Identify the preparation type.
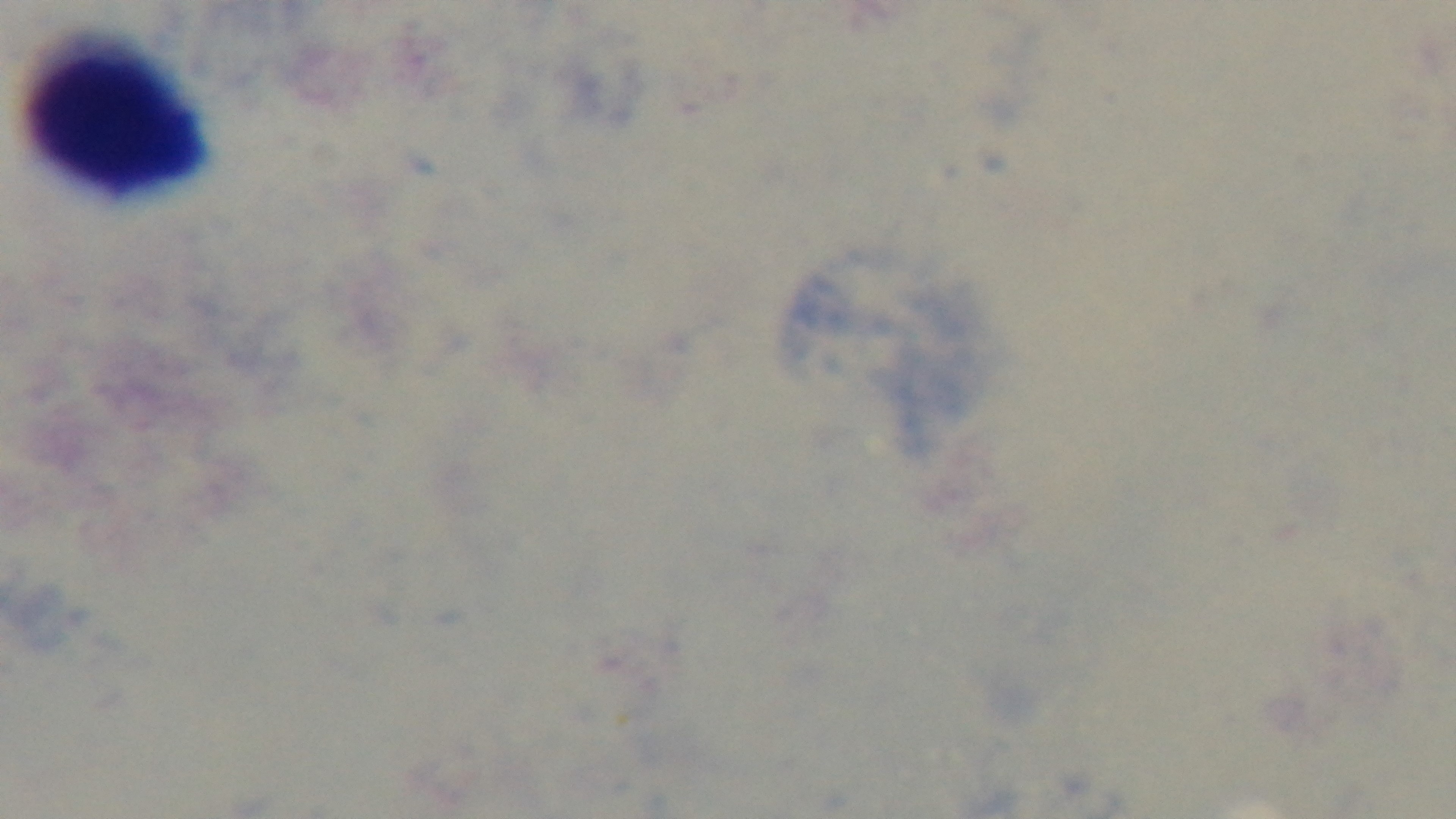

A thick smear.

Malaria status: negative. Giemsa-stained. One field from the slide. Light microscopy. Mounted 4K digital camera. Oil-immersion objective, 100x.